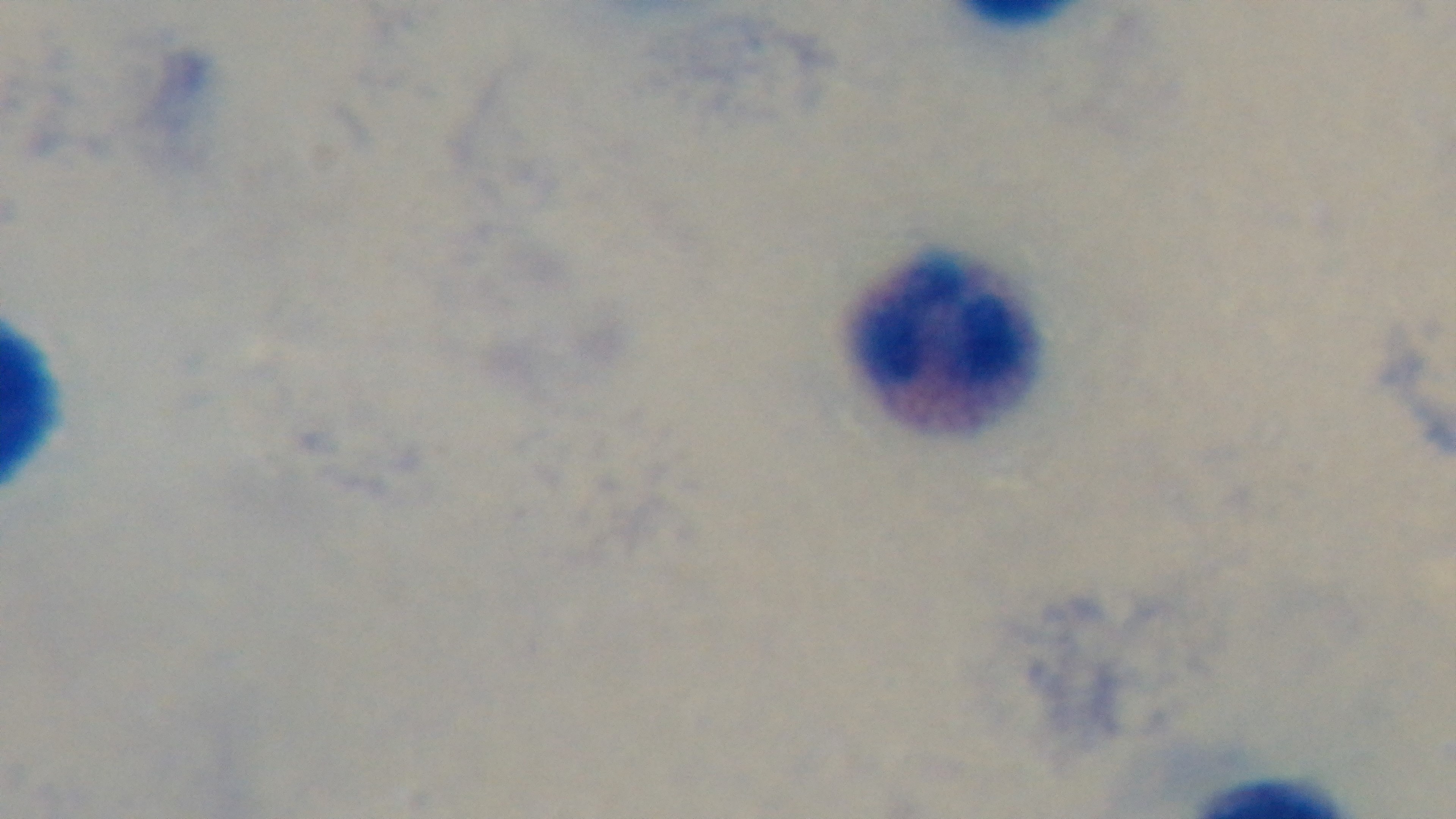

Captured with a mounted 4K digital camera. Giemsa stain. Malaria status: negative. One field from the slide. Preparation: thick smear. 100x oil-immersion objective. Light microscopy.